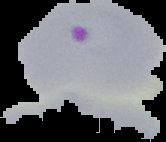

Summary:
  - Image type: segmented cell region on a black background
  - Image size: 166×142 pixels
  - Result: Plasmodium parasites identified
  - Preparation: thin blood smear